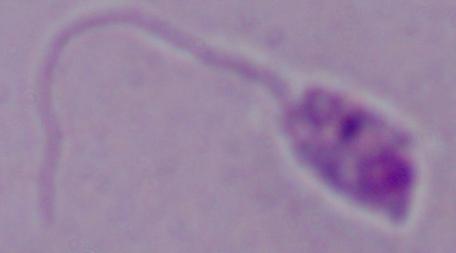
Summary:
  - Magnification: 1000x
  - Identification: Leishmania
  - Modality: micrograph